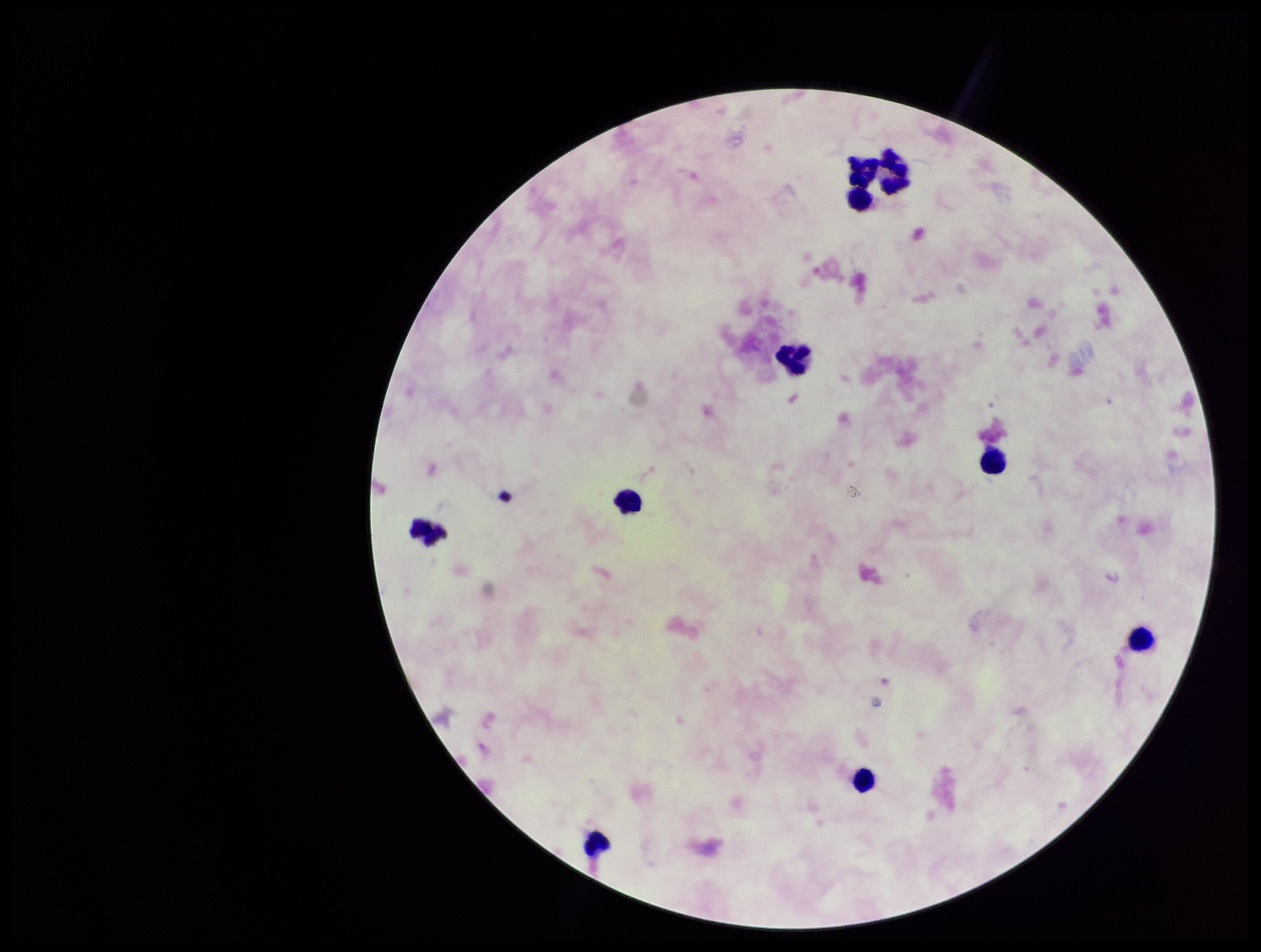

Summary:
  - Patient malaria status: negative
  - Preparation: thick
  - Stain: Giemsa
  - Capture: smartphone photograph through the microscope eyepiece
  - Image size: 1261×952 pixels
  - Field of view: one from this slide
  - Plasmodium parasites: none identified
  - Leukocyte count: 10
  - Parasite count: 0